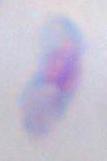

magnification: 1000x
modality: photomicrograph
identification: Toxoplasma gondii